Report the malaria status.
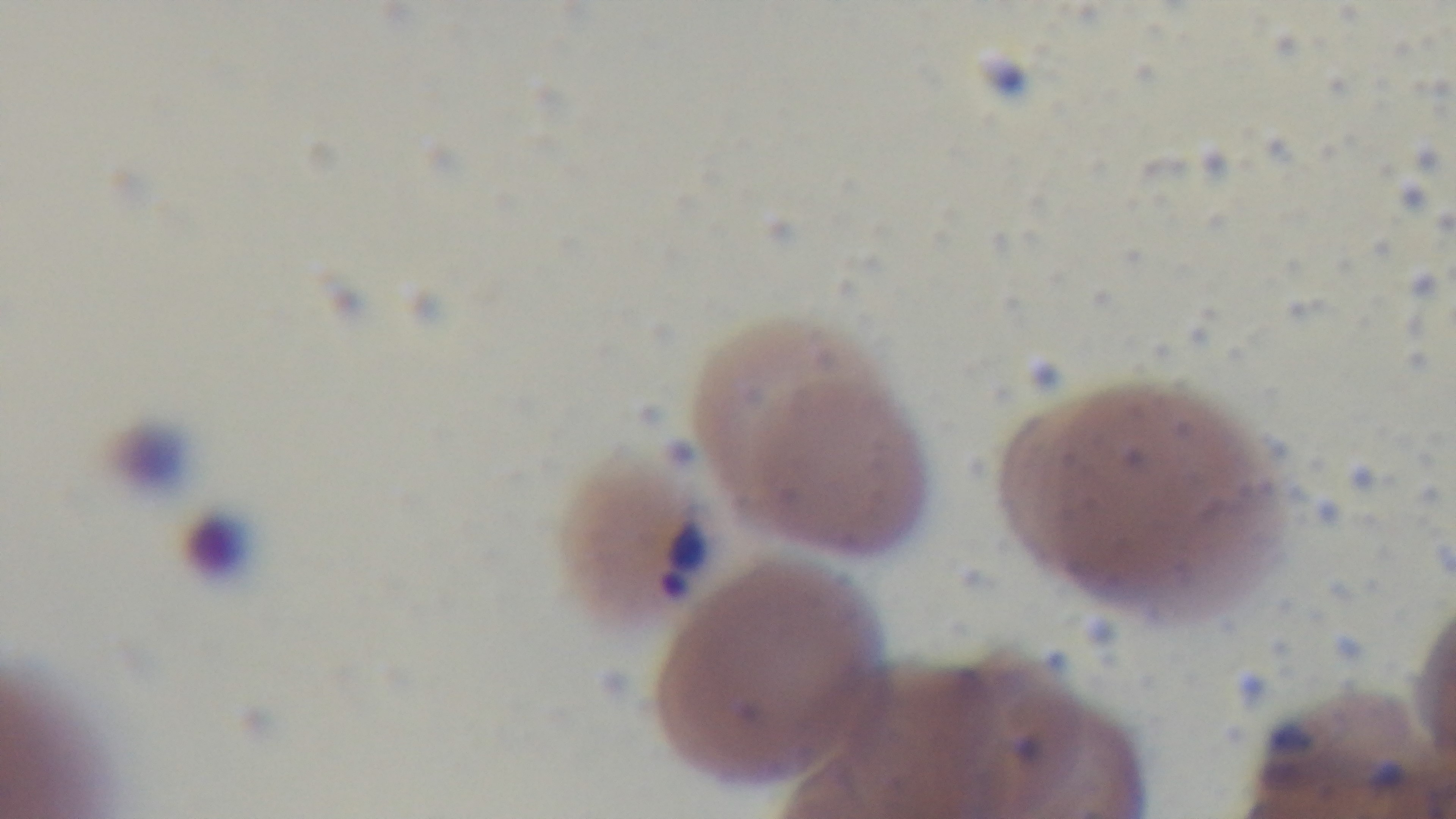

Positive.

Summary:
  - Modality: light microscopy
  - Capture: mounted 4K digital camera
  - Preparation: thin smear
  - Objective: 100x oil immersion
  - Field of view: single
  - Stain: Giemsa